Assess this cell for malaria.
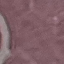
Uninfected.

preparation: thin blood smear
stain: Giemsa
image_type: automatically extracted cell patch, resized to 64 × 64 pixels
capture: smartphone through the microscope eyepiece